Identify the blood parasite species.
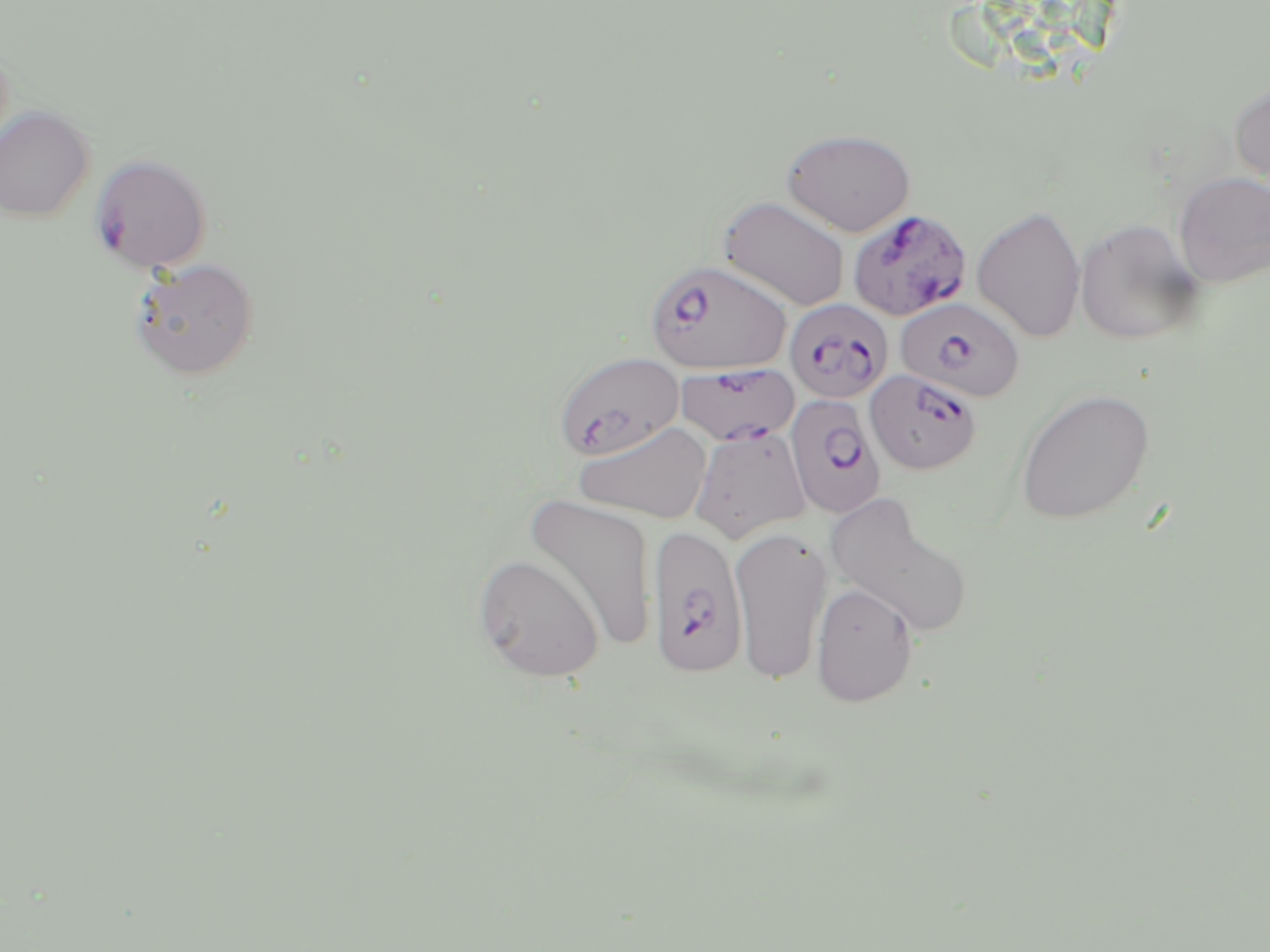

Plasmodium falciparum.

Approximate bounding boxes as named x1/y1/x2/y2 corners in pixels. Plasmodium falciparum-infected red blood cell locations: (x1=849, y1=211, x2=973, y2=323), (x1=644, y1=258, x2=792, y2=375), (x1=896, y1=297, x2=1025, y2=403), (x1=785, y1=298, x2=893, y2=403), (x1=561, y1=357, x2=689, y2=463), (x1=676, y1=362, x2=799, y2=446), (x1=865, y1=368, x2=983, y2=475), (x1=785, y1=394, x2=886, y2=518), (x1=689, y1=422, x2=815, y2=542), (x1=647, y1=523, x2=748, y2=678). Uninfected red blood cell locations: (x1=1229, y1=79, x2=1270, y2=191), (x1=0, y1=106, x2=94, y2=222), (x1=781, y1=128, x2=916, y2=236), (x1=90, y1=153, x2=213, y2=274), (x1=1173, y1=171, x2=1270, y2=289), (x1=719, y1=197, x2=849, y2=311), (x1=971, y1=205, x2=1086, y2=343), (x1=1075, y1=217, x2=1204, y2=344), (x1=128, y1=257, x2=259, y2=380), (x1=1015, y1=388, x2=1154, y2=525), (x1=573, y1=421, x2=713, y2=524), (x1=524, y1=493, x2=657, y2=651), (x1=826, y1=501, x2=972, y2=639), (x1=730, y1=525, x2=832, y2=685), (x1=472, y1=553, x2=605, y2=682), (x1=811, y1=582, x2=919, y2=708). 1000x magnification. Image is 1270×952 pixels. Light microscopy. Single field of view. Thin blood film. May-Grünwald-Giemsa stain.